Assess for malaria.
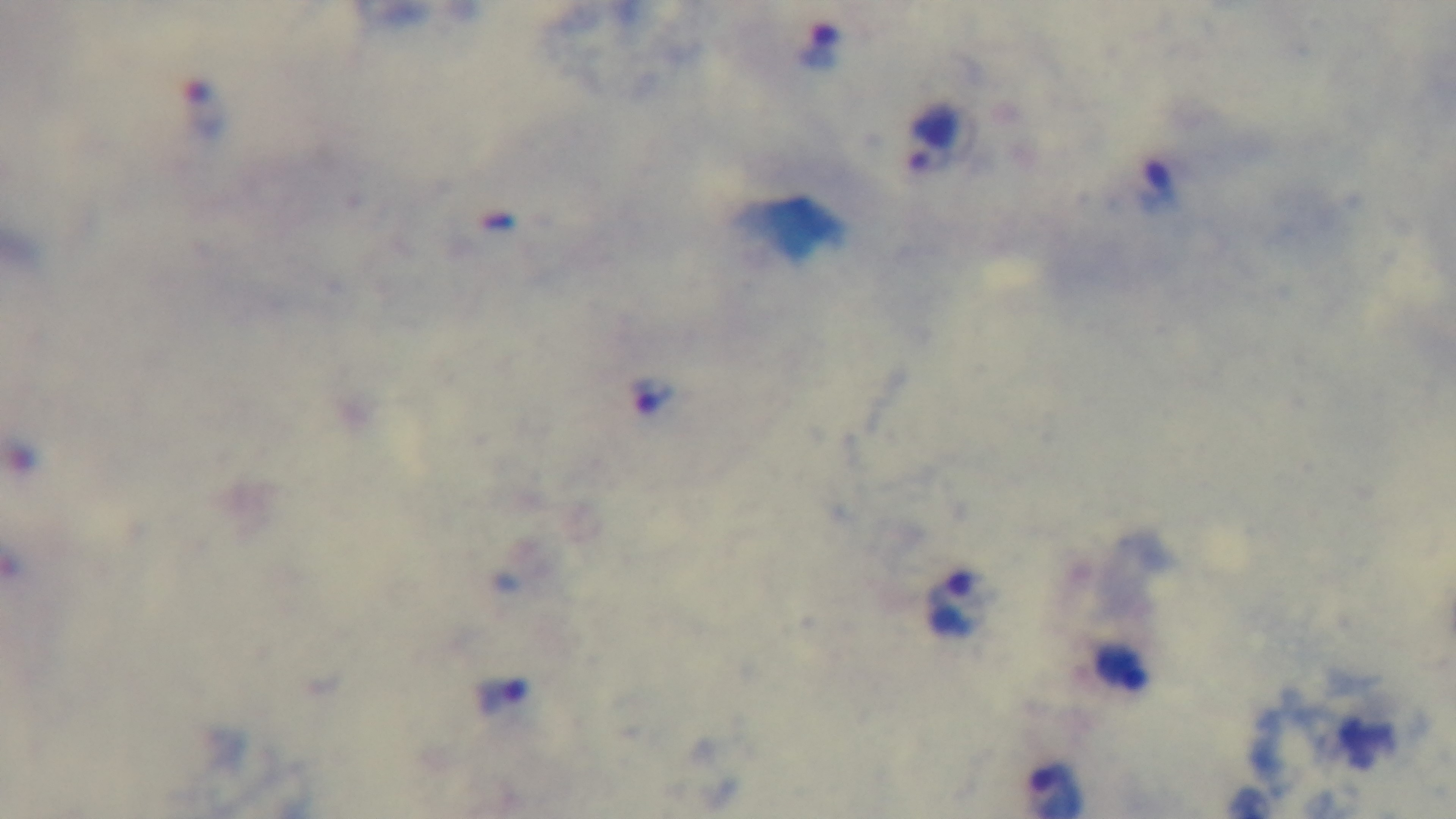
Positive.

stain: Giemsa
capture: mounted 4K digital camera
preparation: thick blood film
modality: light microscopy
objective: 100x oil immersion
field_of_view: one from the slide